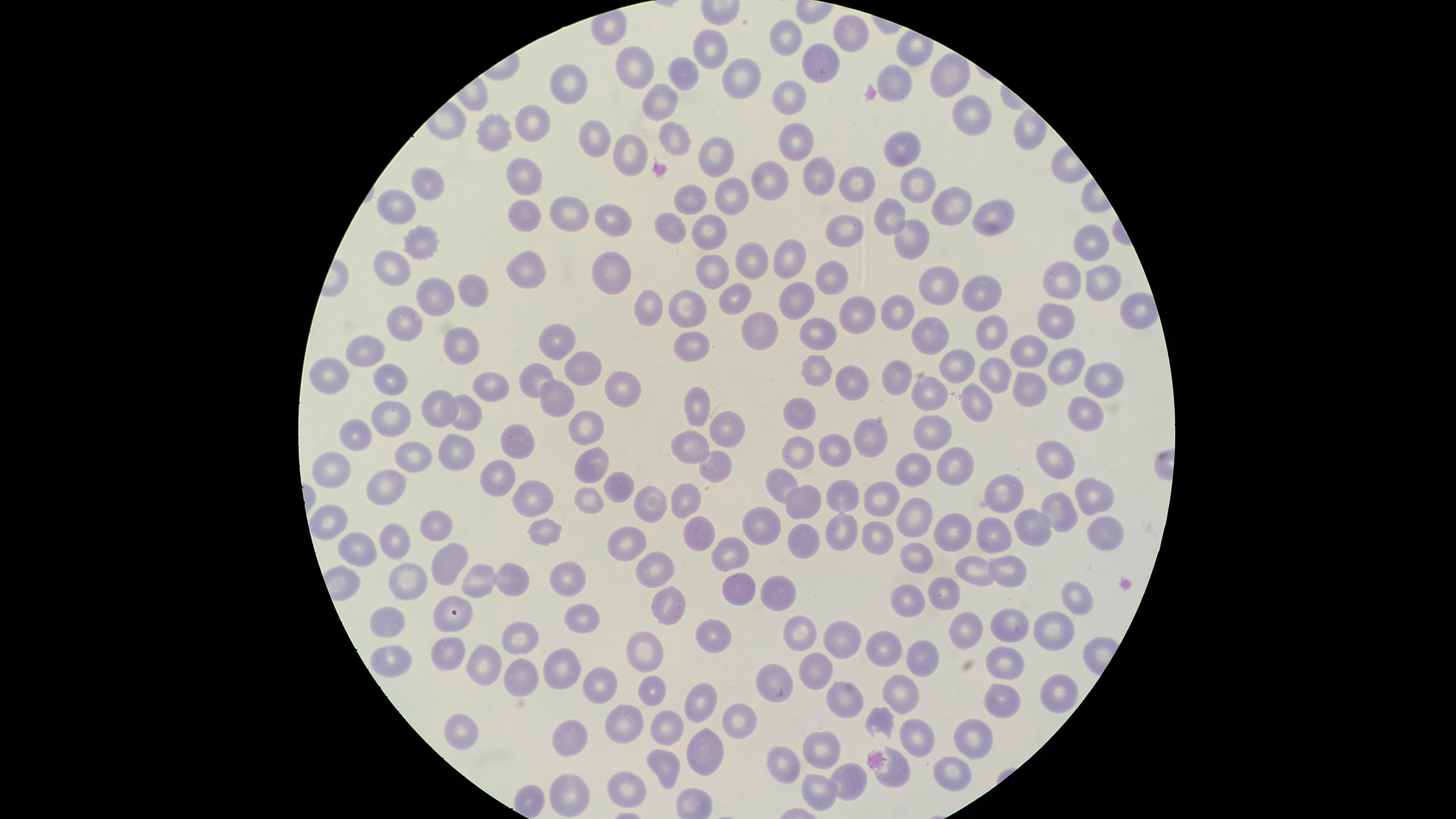
Approximate marker points as {x, y} in pixels. Uninfected red blood cells: {848, 33}, {793, 38}, {715, 52}, {819, 62}, {641, 70}, {687, 75}, {744, 75}, {949, 76}, {895, 82}, {568, 85}, {791, 96}, {660, 104}, {966, 113}, {531, 123}, {499, 135}, {587, 140}, {799, 140}, {680, 142}, {903, 148}, {635, 149}, {710, 156}, {817, 174}, {523, 178}, {771, 181}, {919, 182}, {850, 185}, {428, 188}, {729, 192}, {681, 204}, {958, 207}, {393, 208}, {559, 209}, {519, 213}, {615, 218}, {894, 218}, {990, 220}, {671, 224}, {850, 230}, {710, 232}, {910, 238}, {427, 243}, {1090, 243}, {751, 253}, {787, 259}, {524, 260}, {397, 262}, {616, 266}, {707, 268}, {829, 272}, {1095, 281}, {1069, 282}, {929, 285}, {975, 289}, {736, 292}, {466, 293}, {430, 297}, {797, 297}, {687, 307}, {854, 311}, {655, 312}, {896, 312}, {751, 320}, {1051, 323}, {404, 324}, {992, 332}, {818, 334}, {925, 335}, {557, 343}, {692, 346}, {1032, 349}, {453, 350}, {368, 352}, {963, 363}, {1069, 364}, {581, 366}, {811, 367}, {331, 373}, {892, 374}, {535, 375}, {994, 376}, {849, 377}, {1100, 377}, {394, 383}, {492, 383}, {1032, 385}, {626, 391}, {929, 394}, {566, 398}, {979, 401}, {1084, 407}, {442, 409}, {694, 409}, {801, 410}, {466, 412}, {393, 418}, {728, 421}, {363, 430}, {585, 433}, {936, 434}, {510, 436}, {871, 436}, {690, 445}, {455, 447}, {799, 448}, {836, 449}, {414, 452}, {1046, 452}, {591, 461}, {717, 464}, {955, 464}, {912, 466}, {501, 469}, {339, 470}, {783, 485}, {620, 488}, {390, 489}, {1006, 494}, {878, 496}, {532, 497}, {686, 497}, {842, 497}, {1087, 497}, {588, 501}, {808, 504}, {642, 505}, {1057, 511}, {914, 518}, {329, 521}, {763, 521}, {1030, 524}, {435, 528}, {543, 528}, {839, 531}, {871, 532}, {953, 533}, {1102, 533}, {701, 535}, {987, 537}, {805, 538}, {395, 540}, {357, 548}, {634, 549}, {913, 555}, {737, 557}, {448, 560}, {972, 565}, {655, 568}, {1005, 569}, {566, 573}, {511, 576}, {412, 584}, {470, 584}, {775, 584}, {742, 595}, {940, 595}, {1074, 596}, {903, 602}, {666, 604}, {585, 618}, {446, 619}, {389, 624}, {1013, 627}, {973, 631}, {1052, 631}, {802, 634}, {841, 636}, {713, 639}, {518, 640}, {880, 650}, {445, 652}, {645, 656}, {918, 659}, {387, 662}, {560, 662}, {998, 662}, {817, 665}, {488, 666}, {523, 675}, {782, 679}, {596, 681}, {1057, 687}, {649, 693}, {899, 695}, {845, 699}, {706, 707}, {998, 708}, {737, 718}, {880, 721}, {464, 722}, {628, 723}, {673, 723}, {971, 741}, {916, 743}, {578, 744}, {813, 754}, {696, 755}, {783, 762}, {950, 767}, {668, 768}, {892, 771}, {843, 779}, {631, 785}, {568, 789}, {819, 793}. Giemsa-stained preparation. Presence: no malaria parasites detected. One field of view of the specimen. Image is 1456×819 pixels. Thin smear of blood. Circular visible region. Photographed with a smartphone camera through the microscope eyepiece.